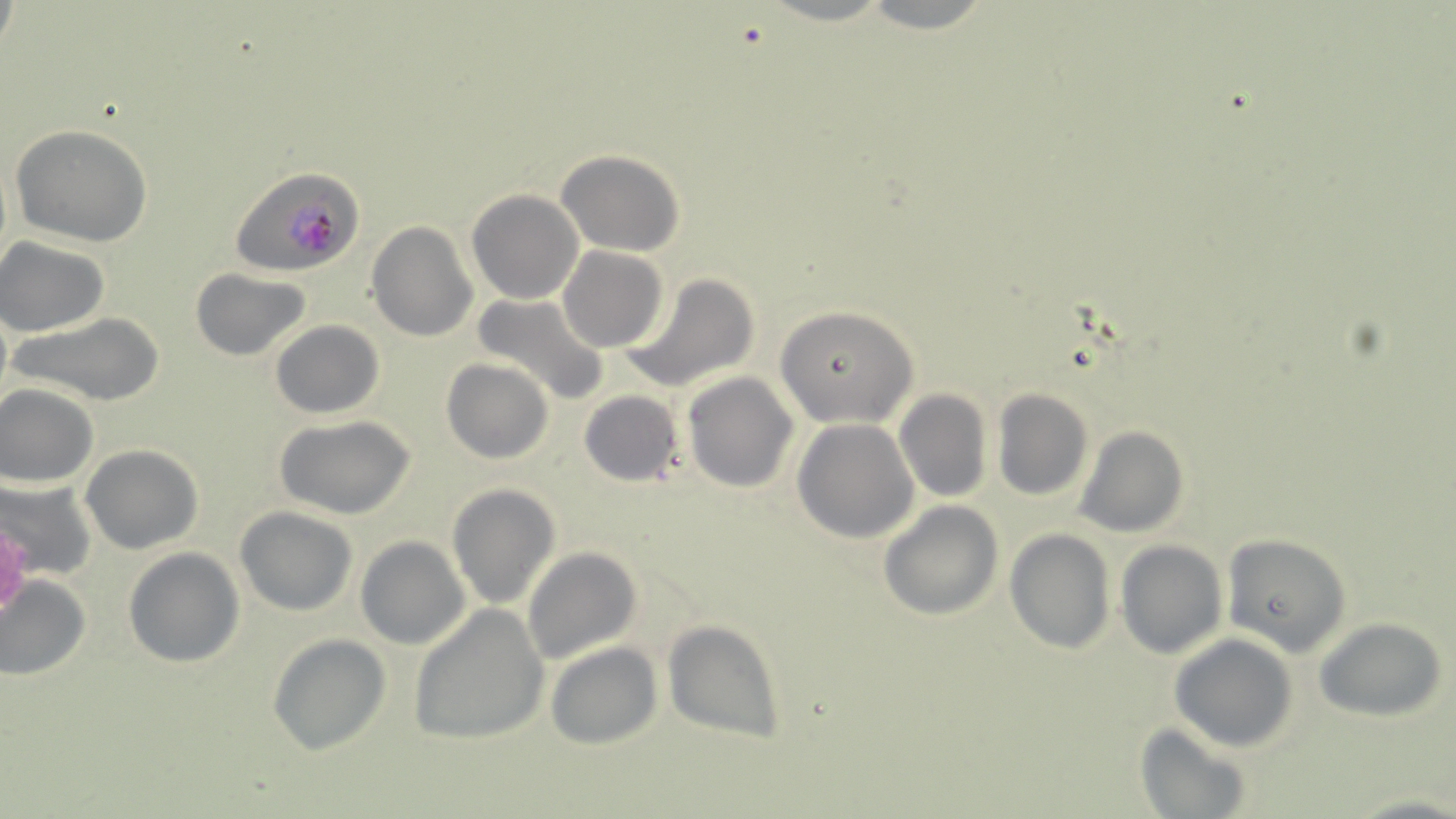
Approximate bounding boxes as (x1, y1, x2, y2) in pixels. Plasmodium falciparum-infected red blood cell locations: (231, 166, 365, 277). Platelet locations: (0, 521, 31, 617). Uninfected red blood cell locations: (858, 0, 995, 34), (9, 124, 154, 246), (555, 149, 686, 257), (466, 189, 583, 304), (366, 221, 478, 343), (0, 237, 113, 336), (557, 246, 668, 353), (190, 268, 312, 361), (621, 272, 760, 392), (470, 292, 609, 408), (0, 301, 12, 411), (774, 305, 919, 428), (9, 313, 166, 407), (270, 320, 384, 419), (441, 359, 552, 465), (683, 372, 798, 493), (0, 385, 98, 486), (991, 388, 1093, 501), (895, 389, 992, 503), (578, 390, 685, 487), (274, 415, 416, 520), (792, 419, 919, 543), (1074, 425, 1188, 538), (80, 444, 203, 553), (0, 478, 98, 581), (446, 483, 561, 610), (878, 500, 1004, 621), (234, 506, 358, 616), (1005, 528, 1117, 654), (1219, 532, 1352, 657), (355, 536, 471, 650), (1114, 540, 1228, 658), (522, 545, 642, 665), (122, 547, 245, 668), (0, 575, 91, 682), (408, 605, 549, 746), (1314, 615, 1450, 722), (662, 619, 787, 747), (267, 633, 391, 755), (1170, 633, 1298, 753), (545, 641, 663, 750), (1133, 722, 1252, 819). Slide-level diagnosis: Plasmodium falciparum. Single field of view. May-Grünwald-Giemsa stain. Captured at 1000x magnification. Image is 1456×819 pixels. Light microscopy. Thin blood smear.